Assess this cell for malaria.
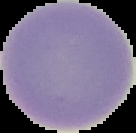
Uninfected.

Summary:
  - Image type: segmented cell region on a black background
  - Preparation: thin blood smear
  - Image size: 136×133 pixels